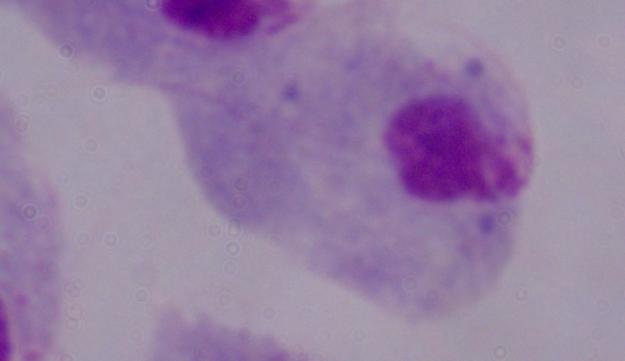

modality = micrograph
identification = trichomonad
magnification = 1000x